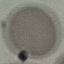

{
  "result": "negative for malaria parasites",
  "preparation": "thin blood film",
  "capture": "smartphone camera at the microscope eyepiece",
  "image_type": "automatically extracted cell patch, resized to 64 × 64 pixels",
  "stain": "Giemsa"
}